Identify the preparation type.
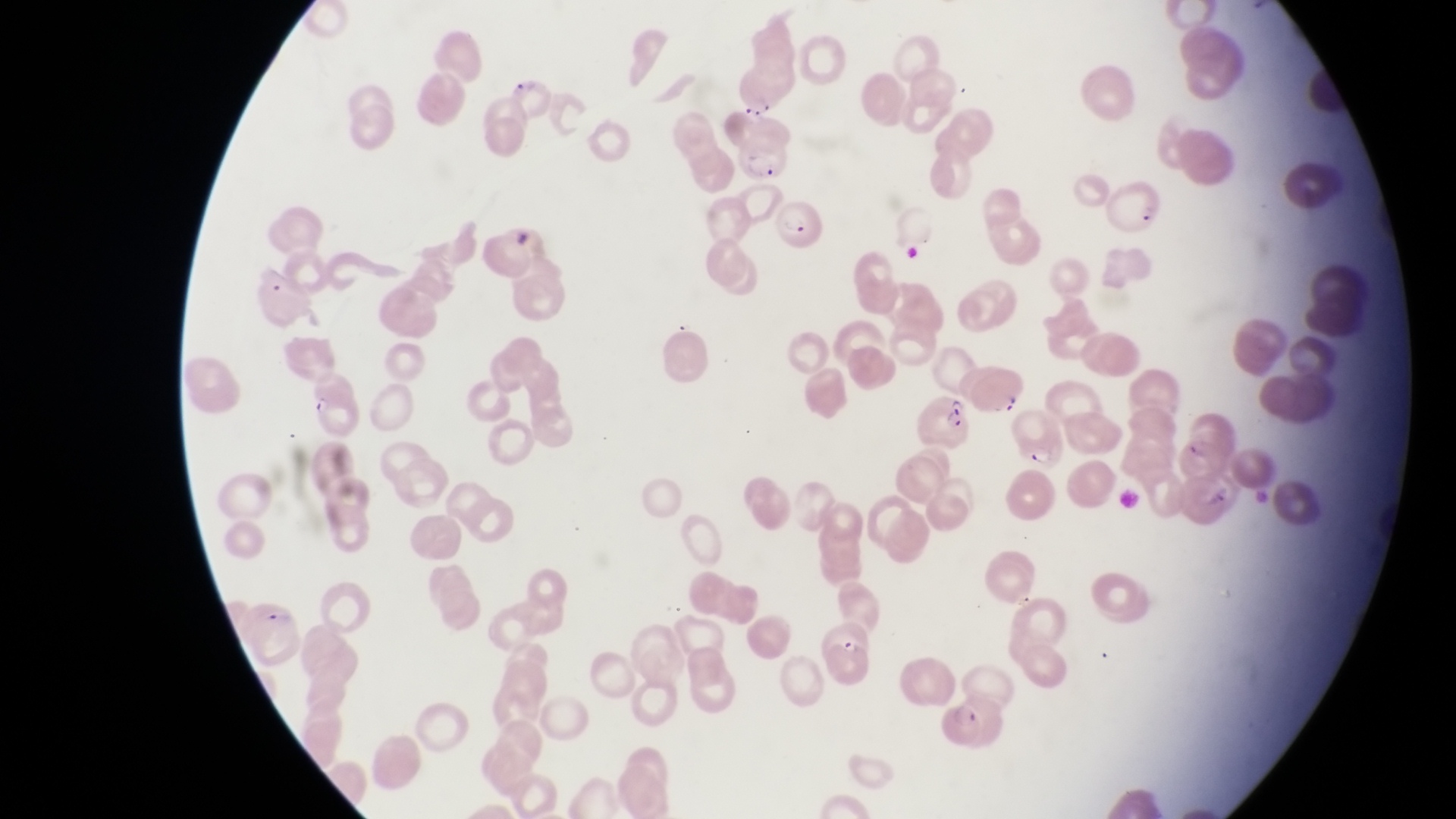

This is a thin smear.

Approximate bounding boxes as (left, top, right, bottom) in pixels.
Summary:
  - Parasitised red blood cell locations: (504, 76, 559, 126), (732, 133, 788, 189), (1100, 179, 1159, 239), (769, 199, 821, 254), (253, 267, 319, 333), (970, 363, 1028, 422), (915, 394, 976, 450), (1004, 406, 1065, 469), (1171, 426, 1234, 484), (811, 624, 882, 690)
  - Country: Uganda
  - Capture: smartphone photograph through the eyepiece of an Olympus CX-23 microscope
  - Field of view: single
  - Image size: 1456×819 pixels
  - Magnification: 1000x